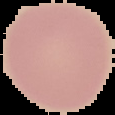 Malaria status: uninfected. The area outside the segmented cell region is set to black. From a thin blood smear. Image is 115×115 pixels.